Identify the parasite.
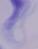

A trypanosome.

Photomicrograph. Captured at 1000x magnification.